Identify the cell.
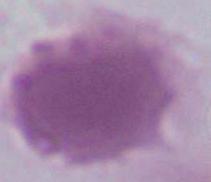
An erythrocyte.

Summary:
  - Magnification: 1000x
  - Modality: micrograph